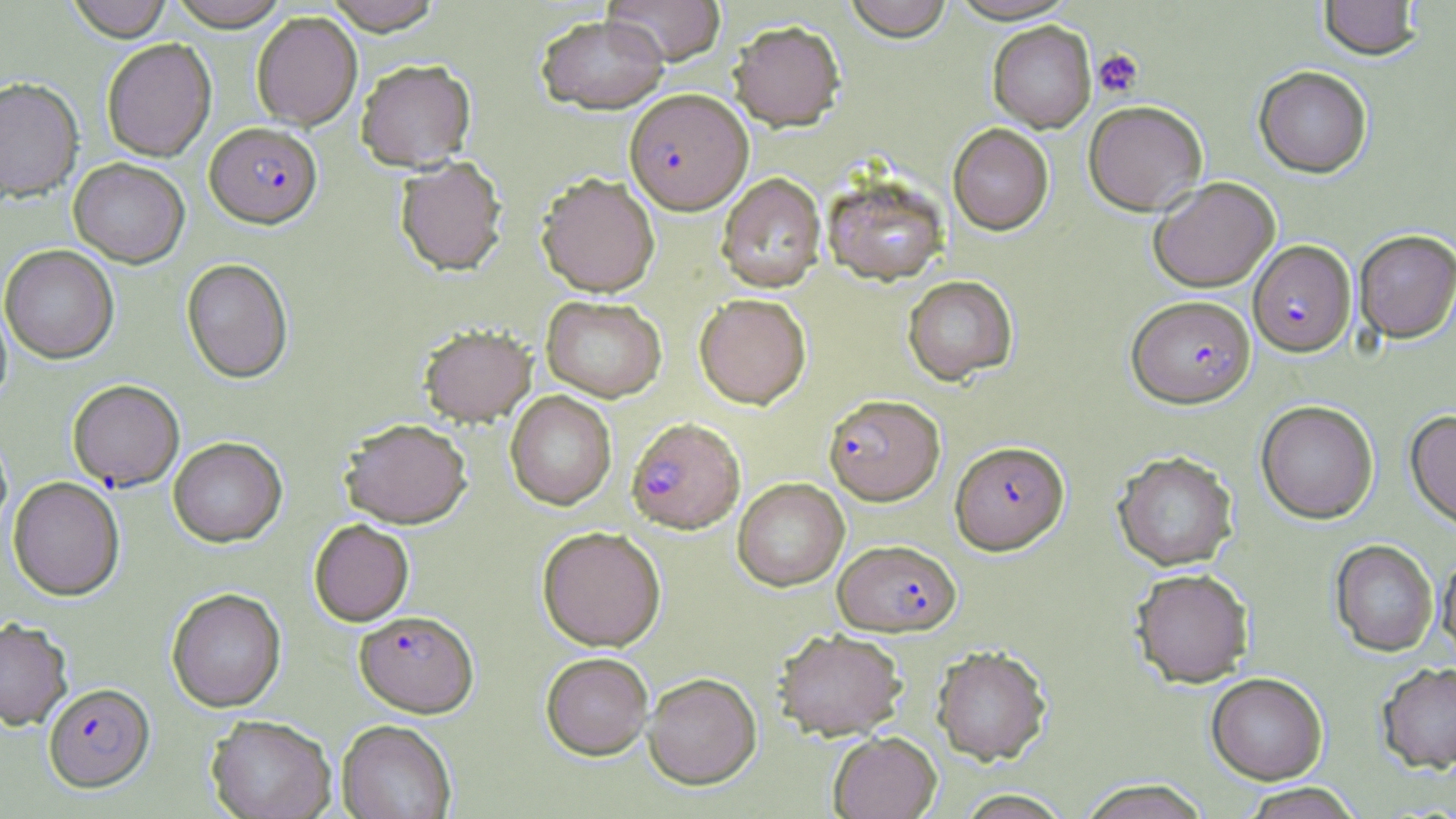
Approximate bounding boxes as (x1,y1)-(x2,y2) corner pairs in pixels. Plasmodium falciparum-infected red blood cell locations: (624,90)-(752,215), (206,122)-(322,228), (1248,239)-(1356,357), (1127,295)-(1255,407), (67,380)-(184,492), (824,394)-(945,506), (626,417)-(745,533), (951,441)-(1069,555), (834,539)-(961,636), (353,611)-(479,718), (43,683)-(155,795). Uninfected red blood cell locations: (66,0)-(172,41), (168,0)-(289,31), (323,0)-(442,35), (603,0)-(726,66), (844,0)-(953,42), (1318,0)-(1422,60), (251,12)-(362,130), (536,14)-(668,114), (729,21)-(846,132), (988,21)-(1096,133), (101,38)-(216,161), (356,58)-(476,172), (1254,65)-(1372,177), (0,77)-(84,202), (1083,100)-(1208,215), (948,123)-(1054,235), (394,156)-(507,277), (69,158)-(189,268), (716,173)-(825,293), (537,174)-(660,297), (822,176)-(948,286), (1148,176)-(1279,293), (1354,230)-(1456,342), (1,245)-(119,364), (181,258)-(293,383), (902,275)-(1018,385), (695,293)-(811,409), (542,297)-(667,402), (0,298)-(12,408), (419,325)-(536,427), (505,391)-(616,511), (1256,400)-(1378,524), (1406,409)-(1456,530), (340,419)-(472,530), (168,437)-(287,548), (1112,450)-(1238,570), (8,477)-(125,601), (733,478)-(849,592), (309,520)-(414,627), (537,528)-(666,653), (1330,539)-(1438,657), (1436,549)-(1456,663), (1130,567)-(1254,687), (167,589)-(286,713), (0,617)-(74,732), (774,629)-(907,740), (932,644)-(1052,765), (541,653)-(654,761), (1376,662)-(1456,773), (1206,672)-(1327,784), (643,674)-(762,790), (206,716)-(337,819), (337,720)-(457,819), (829,731)-(941,819), (1077,779)-(1212,819), (1239,783)-(1364,818), (954,790)-(1074,819). Platelet locations: (1093,48)-(1143,98). Slide-level diagnosis: Plasmodium falciparum. Single field of view. Optical microscopy. Thin blood smear. 1000x magnification. May-Grünwald-Giemsa stain. Image is 1456×819 pixels.